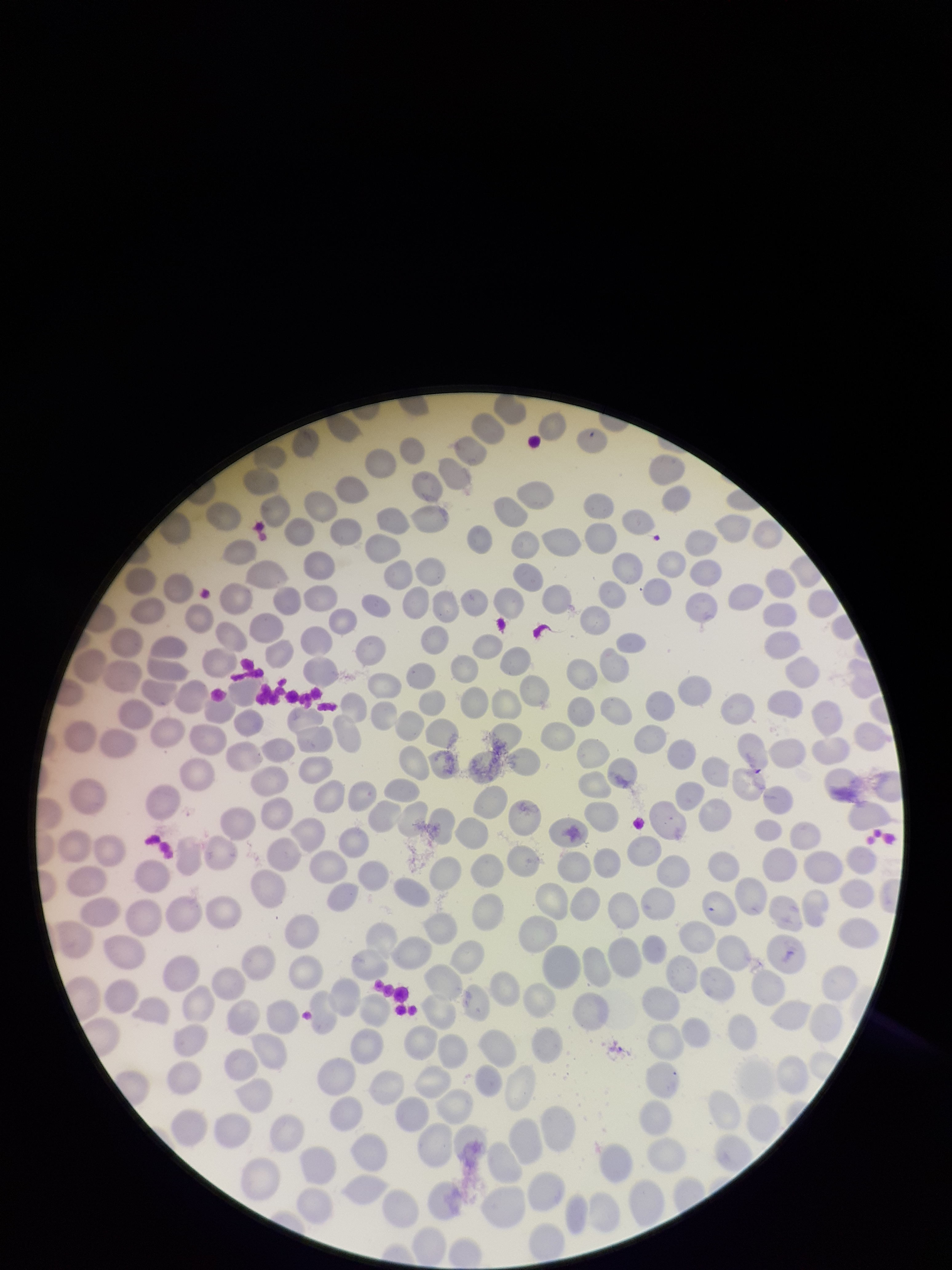

capture = smartphone photograph through the microscope eyepiece
parasitized red blood cells = none identified
stain = Giemsa
parasitized red blood cell count = 0
image size = 952×1270 pixels
patient malaria status = negative
preparation = thin blood smear
red blood cell count = 262
field of view = one from this slide